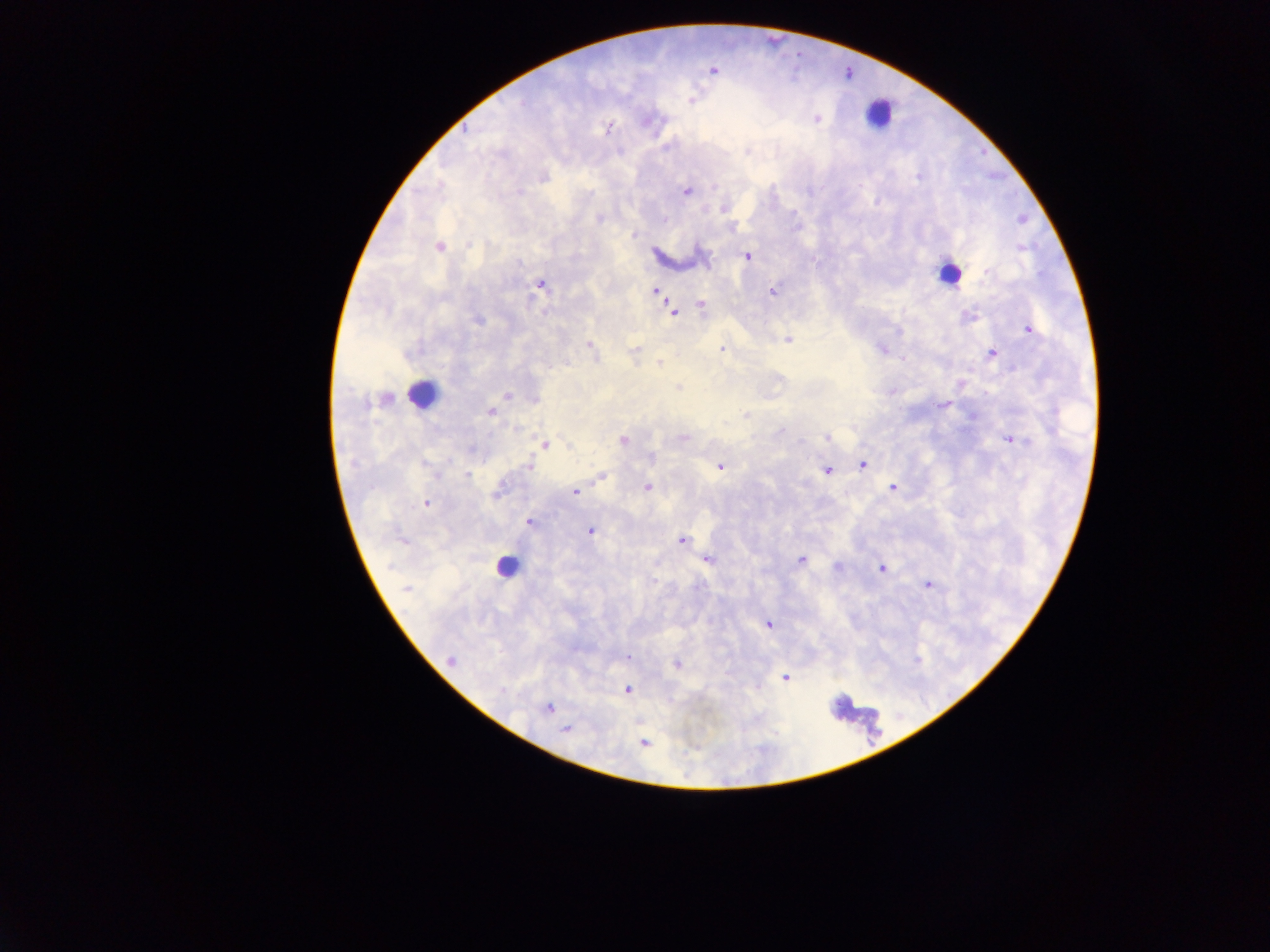
Approximate centers as x y in pixels.
Summary:
  - Object labeled both Plasmodium parasite and leukocyte by the source: 947 274
  - Leukocyte locations: 879 114; 421 394; 506 566
  - Plasmodium parasite locations: 712 70; 691 100; 817 118; 648 121; 607 128; 544 177; 919 177; 519 192; 686 192; 724 209; 600 219; 664 220; 632 235; 439 246; 1021 248; 748 257; 987 271; 540 285; 655 291; 773 292; 701 304; 673 312; 969 317; 479 320; 1028 329; 788 340; 589 346; 722 349; 881 349; 634 350; 992 353; 660 364; 678 387; 506 396; 942 404; 491 412; 746 414; 516 429; 781 430; 683 437; 827 437; 623 440; 1015 440; 544 445; 651 456; 862 464; 529 467; 719 467; 828 470; 467 475; 600 478; 647 487; 893 488; 499 490; 575 492; 426 503; 529 523; 591 531; 401 541; 681 541; 707 560; 801 560; 837 568; 882 569; 928 585; 407 589; 767 624; 629 657; 450 659; 677 665; 785 678; 628 689; 549 707; 565 730; 644 743
  - Preparation: thick blood film
  - Country: Ghana
  - Image size: 1270×952 pixels
  - Field of view: single
  - Capture: mobile-phone photograph through a microscope